State which parasite is depicted.
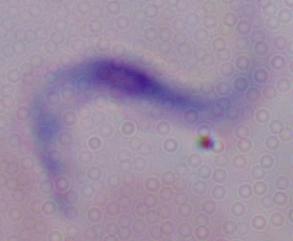
This is a trypanosome.

Summary:
  - Magnification: 1000x
  - Modality: photomicrograph